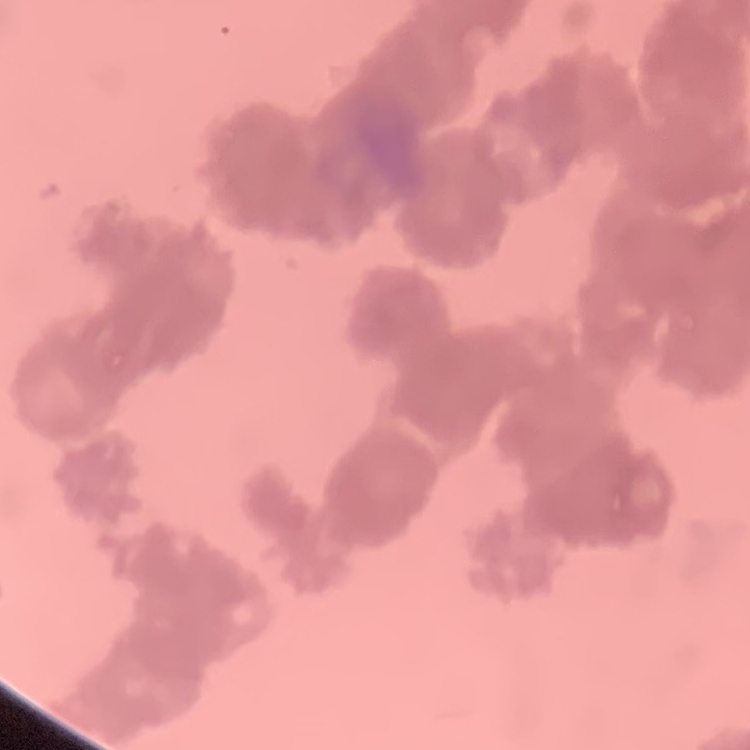

Summary:
  - Erythrocyte morphology: rouleaux formation
  - Image type: one tile cut from a larger photomicrograph
  - Preparation: thin blood smear
  - Stain: Field's or Giemsa